Locate every Plasmodium ovale-infected red blood cell.
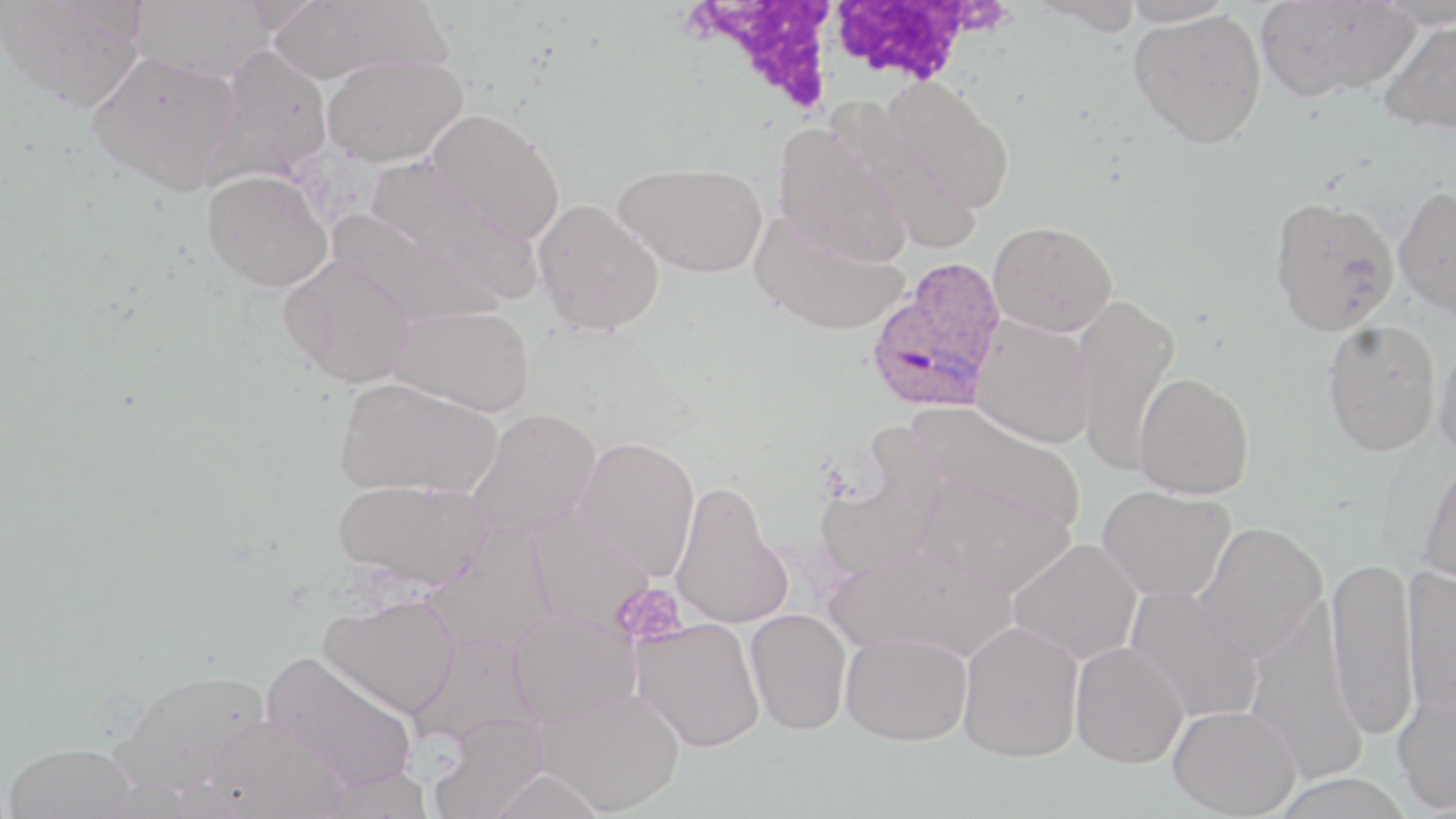

Approximate bounding boxes as [x1, y1, x2, y2] in pixels.
Plasmodium ovale-infected red blood cells: [866, 254, 1008, 409].

Uninfected red blood cell locations: [1, 0, 146, 111], [128, 0, 276, 83], [264, 0, 452, 86], [1120, 0, 1239, 27], [1255, 0, 1419, 101], [1027, 1, 1149, 35], [1375, 1, 1456, 28], [1128, 8, 1267, 149], [1377, 17, 1456, 134], [209, 45, 334, 184], [87, 50, 242, 194], [322, 53, 467, 166], [881, 78, 1016, 214], [835, 100, 985, 254], [426, 109, 565, 244], [772, 126, 912, 268], [364, 159, 540, 302], [614, 160, 768, 277], [202, 169, 332, 292], [1393, 185, 1456, 320], [1268, 196, 1399, 336], [533, 198, 665, 335], [327, 210, 502, 330], [751, 211, 908, 335], [989, 220, 1117, 336], [280, 255, 417, 387], [1071, 292, 1180, 472], [389, 304, 535, 415], [970, 316, 1096, 448], [1321, 318, 1442, 456], [1434, 339, 1456, 461], [1134, 370, 1254, 498], [334, 376, 503, 499], [909, 401, 1087, 534], [466, 408, 601, 541], [574, 435, 701, 580], [814, 451, 943, 582], [1418, 457, 1456, 596], [918, 477, 1077, 596], [332, 478, 493, 590], [672, 480, 791, 630], [1097, 484, 1235, 602], [526, 509, 654, 631], [1193, 521, 1327, 662], [425, 526, 557, 653], [1007, 537, 1143, 665], [826, 544, 1015, 663], [1325, 556, 1418, 739], [1401, 566, 1456, 718], [1125, 586, 1263, 724], [319, 592, 461, 718], [1244, 599, 1365, 784], [508, 608, 640, 727], [744, 609, 852, 735], [632, 618, 765, 751], [958, 621, 1084, 762], [840, 632, 971, 745], [409, 633, 539, 749], [1070, 641, 1188, 768], [262, 651, 418, 793], [110, 668, 269, 800], [534, 685, 685, 815], [1393, 689, 1456, 813], [1167, 705, 1301, 817], [427, 715, 549, 819], [201, 716, 349, 819], [4, 741, 136, 819], [487, 768, 606, 819], [315, 769, 435, 818], [1268, 772, 1414, 819]. Platelet locations: [612, 582, 689, 647]. White blood cell locations: [692, 2, 846, 110], [827, 2, 991, 85]. Slide-level diagnosis: Plasmodium ovale. Thin blood smear. One field of a larger specimen. Captured at 1000x magnification. Optical microscopy. May-Grünwald-Giemsa-stained preparation. Image is 1456×819 pixels.